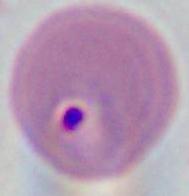
identification = Plasmodium
modality = photomicrograph
magnification = 400x or 1000x